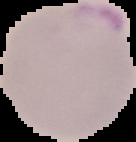 Malaria status: parasitized. The area outside the segmented cell region is set to black. Image is 136×142 pixels. From a thin blood film.